Report the malaria status of this cell.
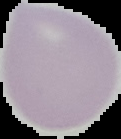

Uninfected.

image type = segmented cell region with the area outside set to black
image size = 121×139 pixels
preparation = thin blood smear